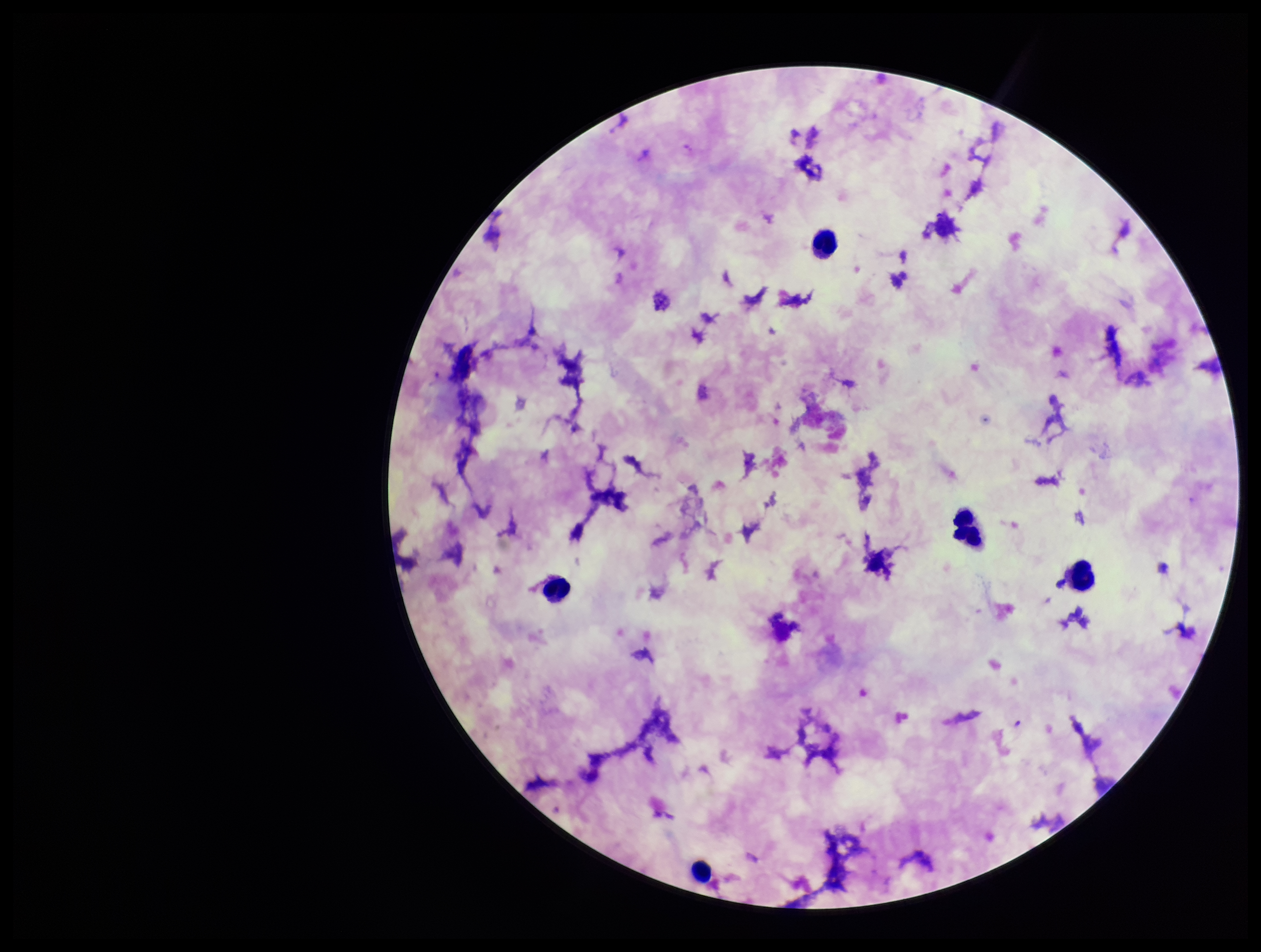
{
  "plasmodium_parasites": "none detected",
  "parasite_count": 0,
  "species_reported_for_this_patient": "Plasmodium falciparum",
  "leukocyte_count": 5,
  "image_size": "1261×952 pixels",
  "field_of_view": "one from this slide",
  "stain": "Giemsa",
  "preparation": "thick smear",
  "patient_malaria_status": "infected",
  "capture": "smartphone photograph through the microscope eyepiece"
}